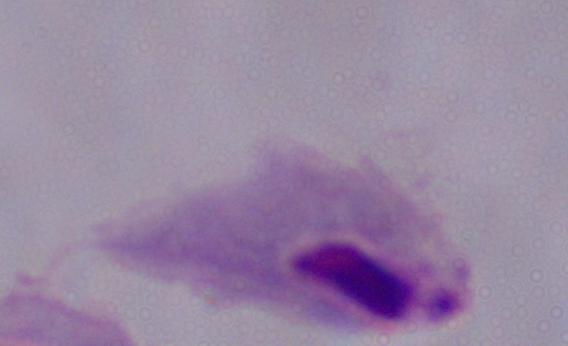

modality = micrograph
magnification = 1000x
identification = trichomonad